Classify this cell by malaria status.
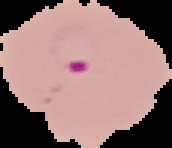

It is parasitized.

preparation: thin blood smear
image_type: cell region segmented out of the field of view; surrounding area masked to black
image_size: 172×148 pixels